Report the malaria status of this cell.
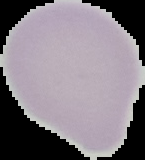
It is uninfected.

preparation: thin blood smear
image_size: 145×160 pixels
image_type: cell region segmented out of the field of view; surrounding area masked to black